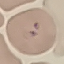

result = no malaria parasites detected
capture = smartphone camera at the microscope eyepiece
stain = Giemsa
preparation = thin smear
image type = cell patch, automatically extracted from a larger field of view and resized to 64 × 64 pixels